Assess the morphology of the erythrocytes.
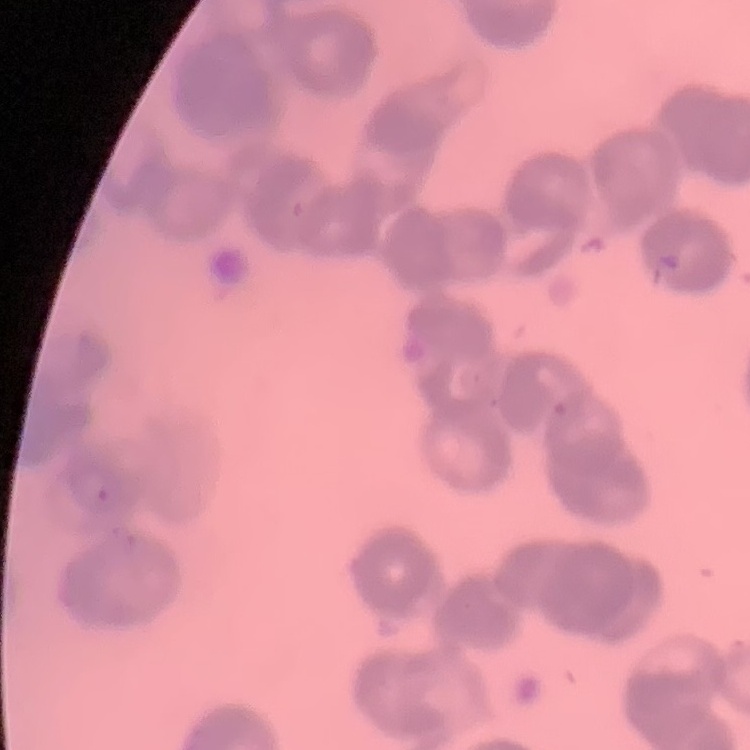

Rouleaux formation.

Summary:
  - Preparation: thin blood film
  - Image type: square crop of a larger photomicrograph
  - Stain: Field's or Giemsa